Classify this cell by malaria status.
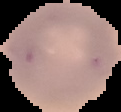
It is uninfected.

Summary:
  - Preparation: thin blood smear
  - Image size: 121×112 pixels
  - Image type: segmented cell region with the area outside set to black